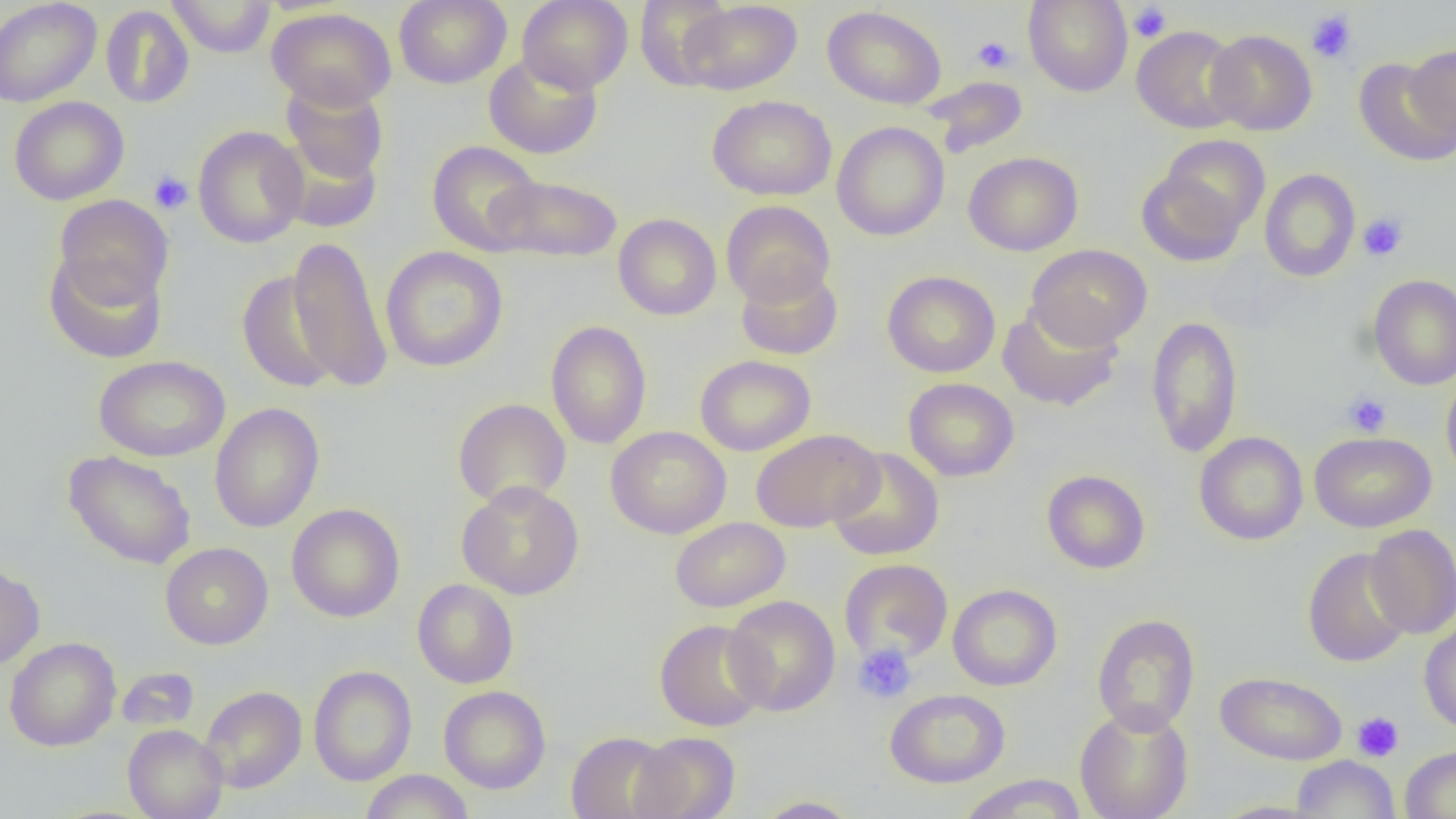
slide-level diagnosis = negative for blood parasites
preparation = thin blood film
field of view = one of a larger specimen
modality = light microscopy
uninfected red blood cell locations = approximate bounding boxes as named x1/y1/x2/y2 corners in pixels: (x1=0, y1=0, x2=102, y2=107), (x1=167, y1=0, x2=276, y2=58), (x1=394, y1=0, x2=512, y2=89), (x1=517, y1=0, x2=633, y2=93), (x1=634, y1=0, x2=734, y2=89), (x1=679, y1=0, x2=802, y2=96), (x1=1023, y1=0, x2=1133, y2=97), (x1=100, y1=5, x2=194, y2=109), (x1=822, y1=5, x2=946, y2=109), (x1=267, y1=7, x2=396, y2=111), (x1=1132, y1=25, x2=1245, y2=134), (x1=1206, y1=29, x2=1317, y2=136), (x1=1406, y1=44, x2=1456, y2=142), (x1=485, y1=52, x2=602, y2=159), (x1=1354, y1=57, x2=1455, y2=166), (x1=924, y1=76, x2=1028, y2=157), (x1=281, y1=79, x2=389, y2=186), (x1=708, y1=95, x2=837, y2=201), (x1=9, y1=96, x2=129, y2=205), (x1=832, y1=121, x2=949, y2=241), (x1=193, y1=125, x2=308, y2=248), (x1=1151, y1=134, x2=1271, y2=239), (x1=270, y1=137, x2=384, y2=232), (x1=427, y1=141, x2=543, y2=255), (x1=963, y1=151, x2=1083, y2=256), (x1=1136, y1=166, x2=1249, y2=267), (x1=1259, y1=169, x2=1360, y2=282), (x1=486, y1=174, x2=623, y2=264), (x1=53, y1=195, x2=174, y2=308), (x1=720, y1=200, x2=836, y2=307), (x1=613, y1=214, x2=721, y2=320), (x1=286, y1=235, x2=393, y2=393), (x1=1026, y1=244, x2=1152, y2=350), (x1=380, y1=246, x2=508, y2=372), (x1=43, y1=251, x2=168, y2=363), (x1=735, y1=265, x2=843, y2=360), (x1=236, y1=270, x2=341, y2=394), (x1=882, y1=270, x2=1000, y2=377), (x1=1368, y1=274, x2=1456, y2=390), (x1=998, y1=303, x2=1123, y2=411), (x1=1146, y1=316, x2=1243, y2=458), (x1=546, y1=320, x2=652, y2=449), (x1=695, y1=354, x2=816, y2=456), (x1=94, y1=355, x2=230, y2=462), (x1=1441, y1=372, x2=1456, y2=484), (x1=903, y1=377, x2=1019, y2=482), (x1=452, y1=398, x2=571, y2=509), (x1=209, y1=403, x2=324, y2=533), (x1=606, y1=426, x2=731, y2=539), (x1=751, y1=429, x2=883, y2=532), (x1=1194, y1=431, x2=1308, y2=545), (x1=1309, y1=432, x2=1436, y2=532), (x1=828, y1=447, x2=944, y2=561), (x1=63, y1=450, x2=197, y2=569), (x1=1042, y1=470, x2=1150, y2=574), (x1=457, y1=481, x2=584, y2=600), (x1=286, y1=503, x2=405, y2=622), (x1=670, y1=517, x2=790, y2=612), (x1=1365, y1=524, x2=1456, y2=639), (x1=160, y1=542, x2=273, y2=649), (x1=1303, y1=547, x2=1413, y2=667), (x1=840, y1=558, x2=953, y2=664), (x1=0, y1=561, x2=45, y2=670), (x1=412, y1=579, x2=519, y2=689), (x1=948, y1=584, x2=1062, y2=690), (x1=723, y1=595, x2=840, y2=716), (x1=1092, y1=614, x2=1200, y2=735), (x1=654, y1=619, x2=770, y2=732), (x1=1419, y1=619, x2=1456, y2=735), (x1=5, y1=636, x2=121, y2=751), (x1=308, y1=665, x2=416, y2=786), (x1=116, y1=667, x2=199, y2=731), (x1=1216, y1=671, x2=1347, y2=765), (x1=199, y1=686, x2=307, y2=793), (x1=438, y1=686, x2=551, y2=794), (x1=884, y1=688, x2=1010, y2=788), (x1=1073, y1=705, x2=1194, y2=819), (x1=123, y1=724, x2=228, y2=819), (x1=567, y1=731, x2=678, y2=819), (x1=630, y1=732, x2=740, y2=819), (x1=1400, y1=745, x2=1456, y2=819), (x1=1292, y1=755, x2=1400, y2=818), (x1=360, y1=770, x2=474, y2=819), (x1=957, y1=774, x2=1088, y2=819), (x1=752, y1=796, x2=862, y2=818), (x1=1209, y1=800, x2=1332, y2=818)
magnification = 1000x
platelet locations = approximate bounding boxes as named x1/y1/x2/y2 corners in pixels: (x1=1129, y1=3, x2=1171, y2=43), (x1=1306, y1=9, x2=1358, y2=63), (x1=972, y1=35, x2=1017, y2=74), (x1=148, y1=170, x2=194, y2=214), (x1=1357, y1=213, x2=1409, y2=261), (x1=1343, y1=392, x2=1391, y2=437), (x1=852, y1=642, x2=917, y2=705), (x1=1352, y1=712, x2=1404, y2=762)
image size = 1456×819 pixels